Classify this cell by malaria status.
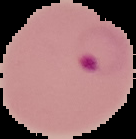
Parasitized.

{
  "preparation": "thin blood smear",
  "image_type": "segmented cell region with the area outside set to black",
  "image_size": "136×139 pixels"
}